Assess this cell for malaria.
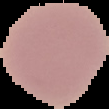
It is uninfected.

preparation = thin blood smear
image type = segmented cell region on a black background
image size = 109×109 pixels